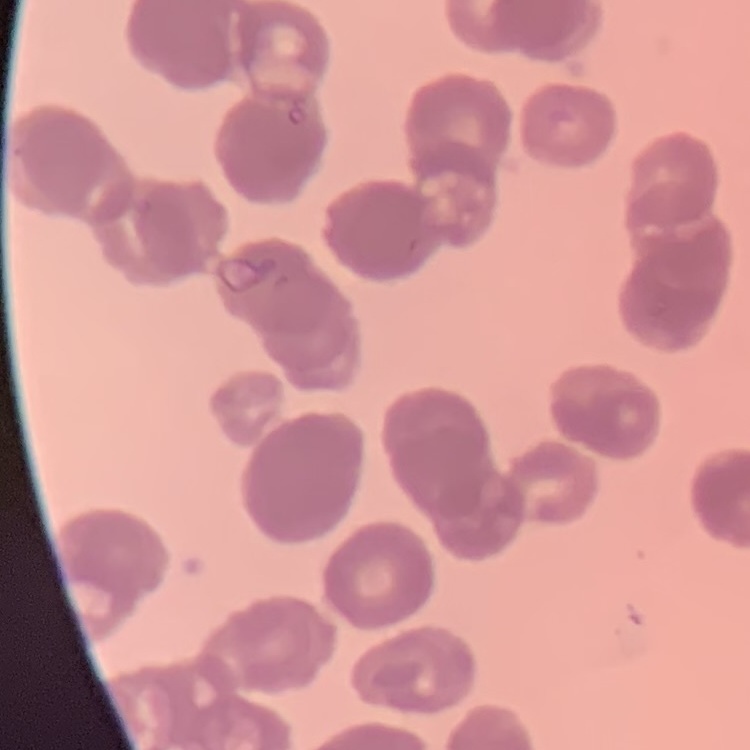

The red blood cells exhibit rouleaux formation. Thin blood film. Square crop of a larger photomicrograph. Stained with either Field's or Giemsa.